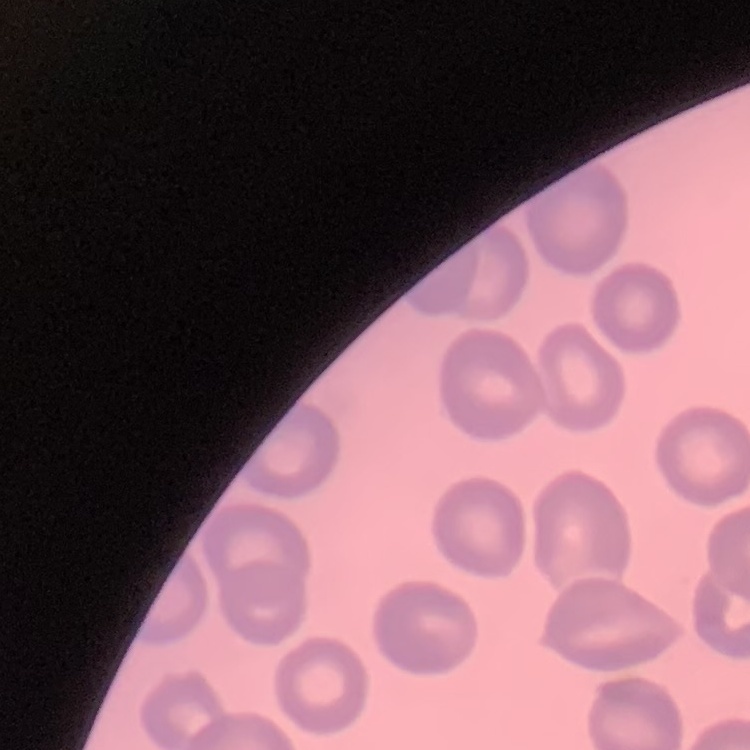
red blood cell morphology = no rouleaux formation
preparation = thin blood film
image type = square crop of a larger photomicrograph
stain = Field's or Giemsa